Locate every uninfected red blood cell.
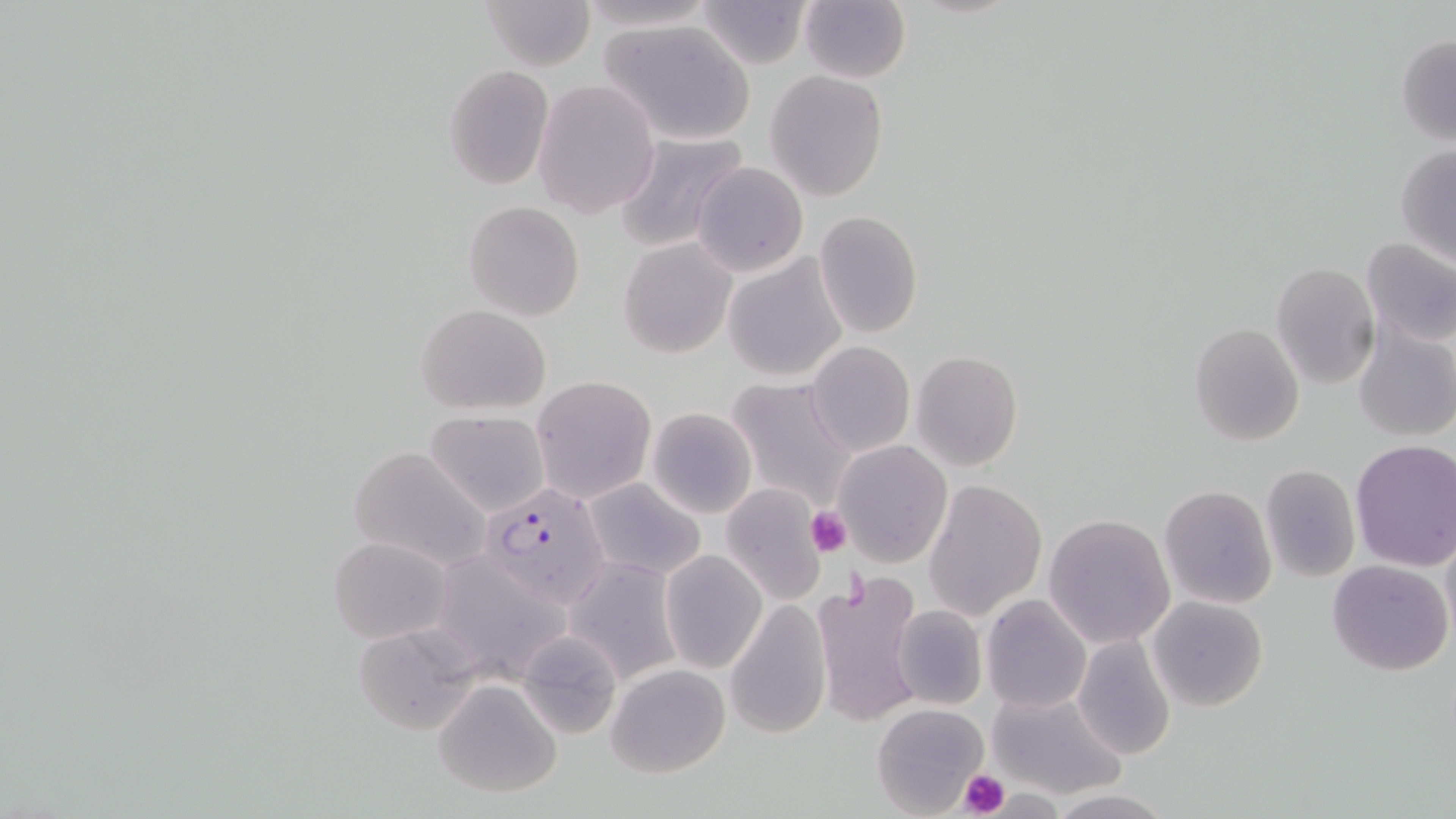

Approximate bounding boxes as named x1/y1/x2/y2 corners in pixels.
Uninfected red blood cells: (x1=478, y1=0, x2=595, y2=70), (x1=581, y1=0, x2=715, y2=31), (x1=697, y1=1, x2=810, y2=68), (x1=798, y1=2, x2=910, y2=83), (x1=598, y1=18, x2=756, y2=147), (x1=1395, y1=35, x2=1456, y2=145), (x1=444, y1=65, x2=553, y2=188), (x1=764, y1=70, x2=890, y2=201), (x1=532, y1=78, x2=660, y2=219), (x1=612, y1=132, x2=750, y2=254), (x1=1395, y1=144, x2=1456, y2=266), (x1=692, y1=161, x2=809, y2=278), (x1=463, y1=201, x2=584, y2=320), (x1=814, y1=211, x2=923, y2=337), (x1=1360, y1=235, x2=1456, y2=348), (x1=617, y1=236, x2=739, y2=360), (x1=722, y1=253, x2=850, y2=385), (x1=1270, y1=261, x2=1380, y2=392), (x1=415, y1=304, x2=553, y2=415), (x1=1353, y1=321, x2=1456, y2=443), (x1=1189, y1=323, x2=1304, y2=446), (x1=807, y1=341, x2=914, y2=456), (x1=911, y1=350, x2=1023, y2=471), (x1=531, y1=375, x2=655, y2=502), (x1=726, y1=378, x2=860, y2=511), (x1=646, y1=406, x2=757, y2=518), (x1=426, y1=411, x2=550, y2=516), (x1=832, y1=439, x2=953, y2=569), (x1=1349, y1=440, x2=1456, y2=574), (x1=350, y1=446, x2=490, y2=571), (x1=1259, y1=463, x2=1360, y2=582), (x1=582, y1=478, x2=703, y2=580), (x1=923, y1=479, x2=1047, y2=620), (x1=721, y1=484, x2=827, y2=605), (x1=1158, y1=484, x2=1277, y2=610), (x1=1043, y1=512, x2=1176, y2=649), (x1=328, y1=535, x2=453, y2=643), (x1=659, y1=550, x2=767, y2=674), (x1=448, y1=552, x2=574, y2=693), (x1=563, y1=556, x2=683, y2=684), (x1=1327, y1=558, x2=1453, y2=676), (x1=812, y1=575, x2=926, y2=729), (x1=980, y1=593, x2=1092, y2=713), (x1=1148, y1=595, x2=1269, y2=711), (x1=725, y1=601, x2=830, y2=740), (x1=892, y1=605, x2=988, y2=711), (x1=350, y1=622, x2=479, y2=733), (x1=515, y1=628, x2=623, y2=739), (x1=1072, y1=634, x2=1176, y2=759), (x1=605, y1=663, x2=730, y2=777), (x1=432, y1=678, x2=563, y2=797), (x1=987, y1=688, x2=1127, y2=799), (x1=872, y1=703, x2=990, y2=817), (x1=1044, y1=791, x2=1179, y2=819).

slide_level_diagnosis: Plasmodium falciparum
modality: light microscopy
platelet_locations: 'approximate bounding boxes as named x1/y1/x2/y2 corners in pixels: (x1=804, y1=505, x2=853, y2=558), (x1=956, y1=769, x2=1011, y2=817)'
preparation: thin blood film
image_size: 1456×819 pixels
field_of_view: single
magnification: 1000x
plasmodium_falciparum_infected_red_blood_cell_locations: 'approximate bounding boxes as named x1/y1/x2/y2 corners in pixels: (x1=482, y1=480, x2=608, y2=605)'
stain: May-Grünwald-Giemsa